Describe the morphology of the erythrocytes.
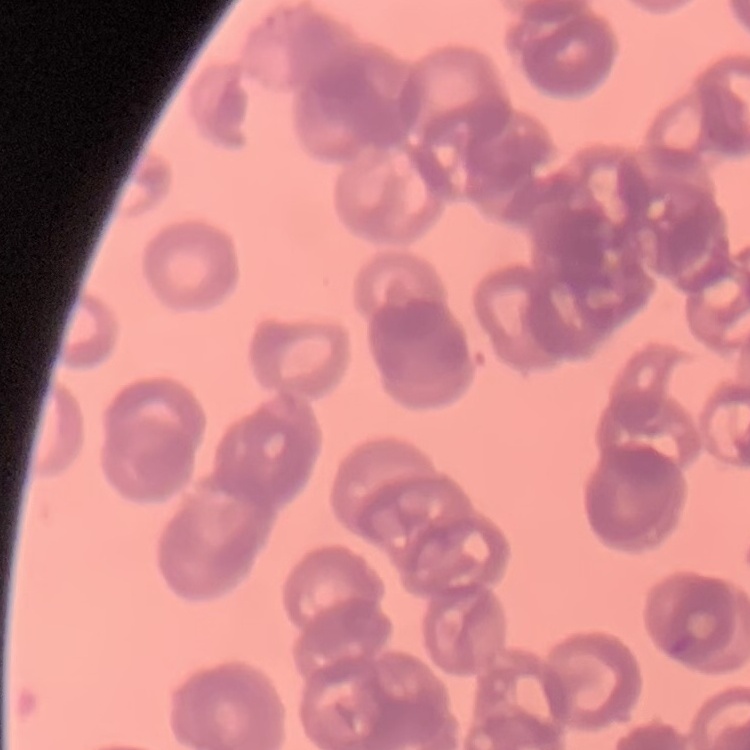
They show rouleaux formation.

Summary:
  - Preparation: thin peripheral smear
  - Image type: square crop of a larger photomicrograph
  - Stain: Field's or Giemsa